State the preparation type.
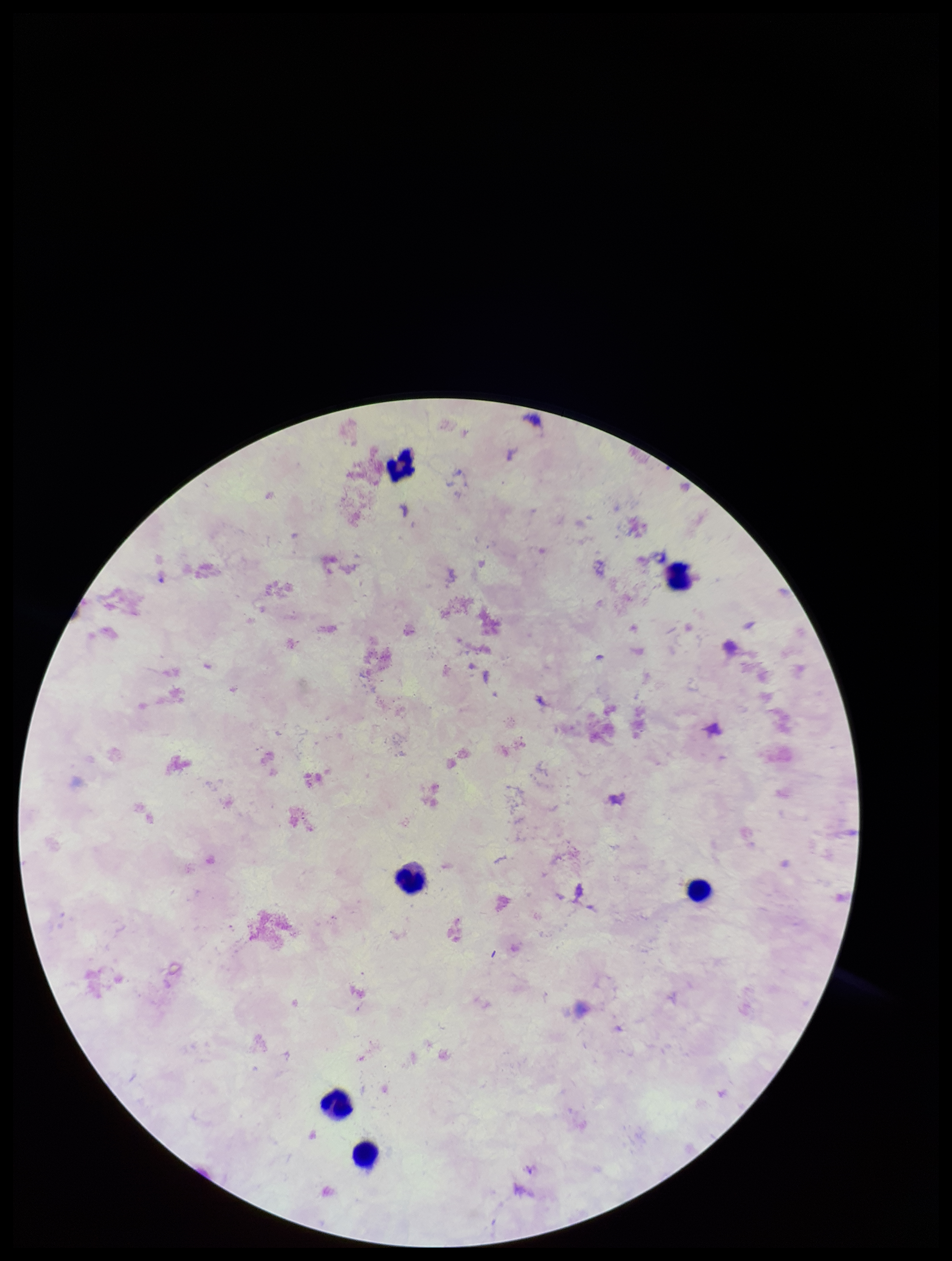
Thick.

patient malaria status = negative
stain = Giemsa
field of view = single
image size = 952×1261 pixels
parasite count = 0
capture = smartphone photograph through the microscope eyepiece
Plasmodium parasites = none seen
leukocyte count = 6